Report the malaria status of this cell.
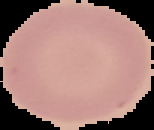

Uninfected.

Summary:
  - Preparation: thin blood smear
  - Image size: 154×130 pixels
  - Image type: cell region segmented out of the field of view; surrounding area masked to black